Locate every blood parasite and identify its species.
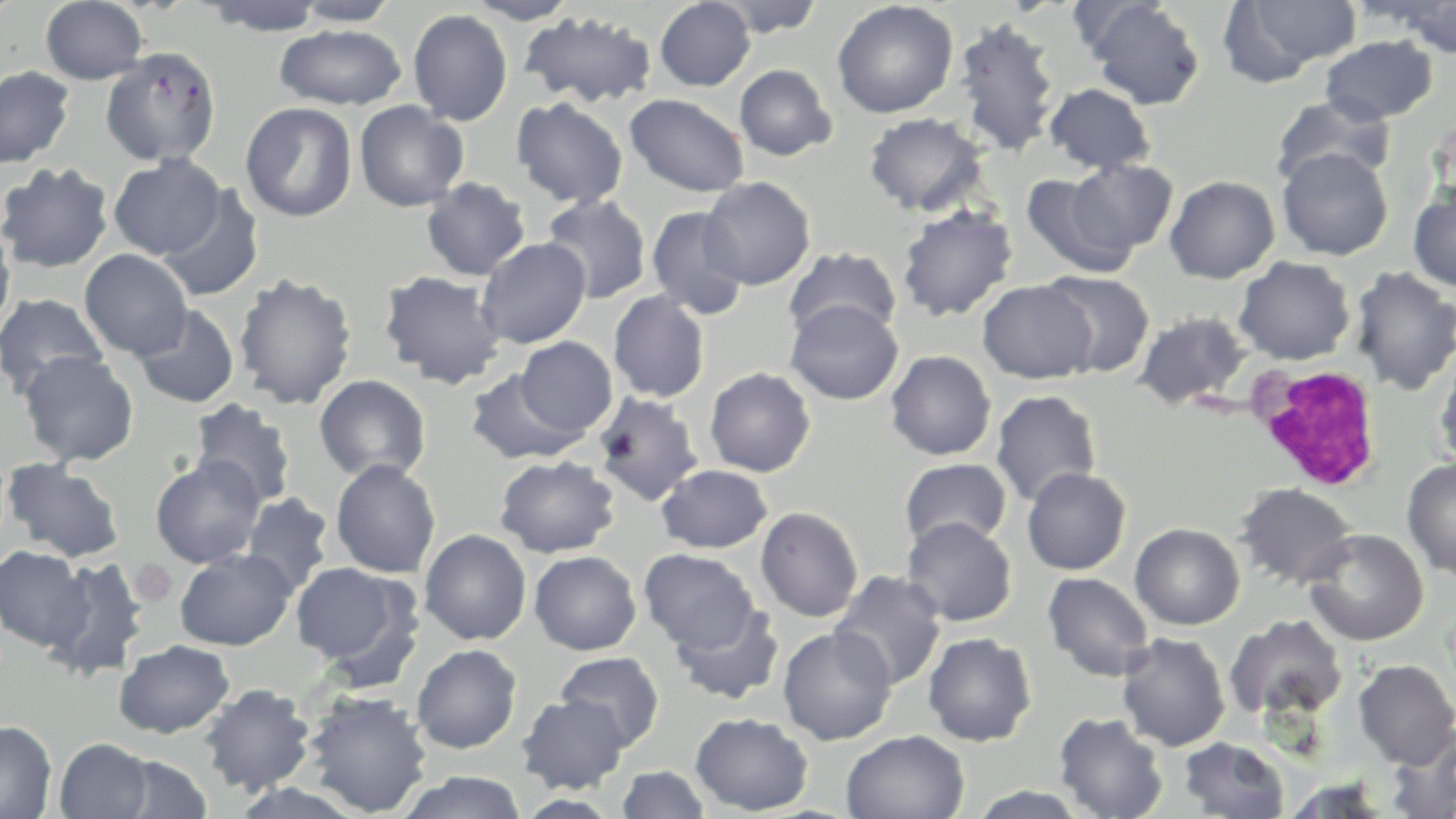
No blood parasites seen.

Approximate bounding boxes as (x1, y1, x2, y2) in pixels. White blood cell locations: (1251, 363, 1383, 491). Uninfected red blood cell locations: (40, 0, 149, 84), (289, 0, 403, 26), (462, 0, 579, 24), (654, 0, 756, 91), (711, 0, 825, 38), (1218, 0, 1362, 84), (0, 1, 21, 26), (199, 1, 330, 36), (832, 1, 958, 118), (1080, 1, 1206, 110), (1381, 1, 1456, 58), (407, 9, 513, 126), (519, 11, 657, 109), (951, 16, 1062, 157), (274, 23, 407, 110), (1320, 35, 1438, 125), (101, 47, 222, 167), (734, 64, 837, 161), (0, 66, 75, 168), (1044, 83, 1156, 174), (1270, 93, 1395, 189), (624, 94, 750, 197), (511, 96, 628, 208), (354, 100, 469, 212), (240, 102, 358, 222), (864, 112, 987, 217), (1276, 147, 1393, 261), (108, 153, 226, 260), (1063, 159, 1179, 260), (0, 161, 115, 273), (1021, 171, 1140, 280), (1165, 175, 1280, 283), (421, 177, 530, 281), (699, 177, 816, 289), (157, 185, 265, 302), (1408, 185, 1456, 291), (541, 194, 652, 304), (896, 204, 1018, 322), (646, 205, 750, 321), (0, 222, 16, 333), (476, 237, 591, 349), (783, 246, 902, 344), (79, 249, 193, 360), (1233, 256, 1355, 365), (1350, 266, 1456, 396), (379, 270, 507, 389), (1040, 270, 1155, 379), (233, 272, 358, 410), (977, 280, 1097, 384), (608, 291, 710, 402), (0, 293, 109, 400), (785, 299, 903, 405), (132, 304, 239, 408), (1133, 311, 1252, 411), (514, 337, 617, 438), (1433, 349, 1456, 474), (18, 350, 139, 466), (886, 350, 996, 460), (705, 367, 816, 477), (465, 368, 587, 464), (314, 374, 431, 483), (991, 389, 1102, 507), (592, 392, 704, 506), (188, 399, 297, 508), (150, 455, 265, 568), (494, 455, 620, 558), (1401, 457, 1456, 580), (900, 458, 1012, 551), (2, 459, 126, 562), (331, 459, 441, 578), (656, 464, 773, 553), (1022, 467, 1131, 575), (1234, 482, 1358, 590), (240, 492, 334, 596), (755, 506, 863, 622), (901, 516, 1017, 627), (1130, 523, 1245, 630), (1302, 527, 1428, 646), (419, 529, 532, 645), (0, 547, 92, 651), (175, 548, 297, 650), (638, 549, 759, 652), (529, 551, 642, 655), (42, 556, 148, 681), (291, 562, 417, 670), (830, 570, 947, 691), (1042, 572, 1155, 682), (669, 601, 785, 706), (1224, 614, 1347, 721), (777, 625, 897, 745), (922, 632, 1037, 746), (1116, 632, 1230, 751), (113, 639, 235, 738), (412, 644, 522, 753), (554, 651, 665, 750), (1352, 659, 1456, 768), (200, 683, 315, 795), (303, 690, 433, 817), (517, 693, 630, 793), (690, 712, 813, 815), (1054, 712, 1169, 818), (0, 720, 57, 818), (1384, 728, 1456, 819), (841, 730, 970, 818), (1179, 737, 1290, 819), (55, 738, 156, 819), (113, 754, 214, 818), (616, 765, 710, 819), (396, 771, 528, 819), (1281, 774, 1395, 818), (223, 781, 371, 819), (960, 785, 1097, 818). Slide-level diagnosis: negative for blood parasites. May-Grünwald-Giemsa stain. Thin blood film. Image is 1456×819 pixels. Single field of view. Light microscopy. 1000x magnification.